Classify this cell by malaria status.
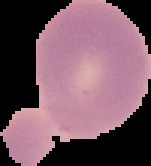
Uninfected.

Image is 151×166 pixels. Cell region segmented out of the field of view; the surrounding area is masked to black. From a thin blood smear.